Identify the cell.
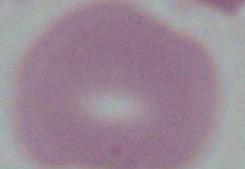
An erythrocyte.

magnification: 1000x
modality: photomicrograph